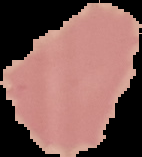

Summary:
  - Result: no Plasmodium parasites detected
  - Preparation: thin blood smear
  - Image size: 142×157 pixels
  - Image type: segmented cell region on a black background